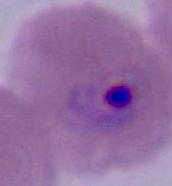

Summary:
  - Modality: photomicrograph
  - Identification: Plasmodium
  - Magnification: 400x or 1000x